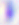
magnification = 400x
identification = Toxoplasma gondii
modality = micrograph